Locate and identify every blood parasite.
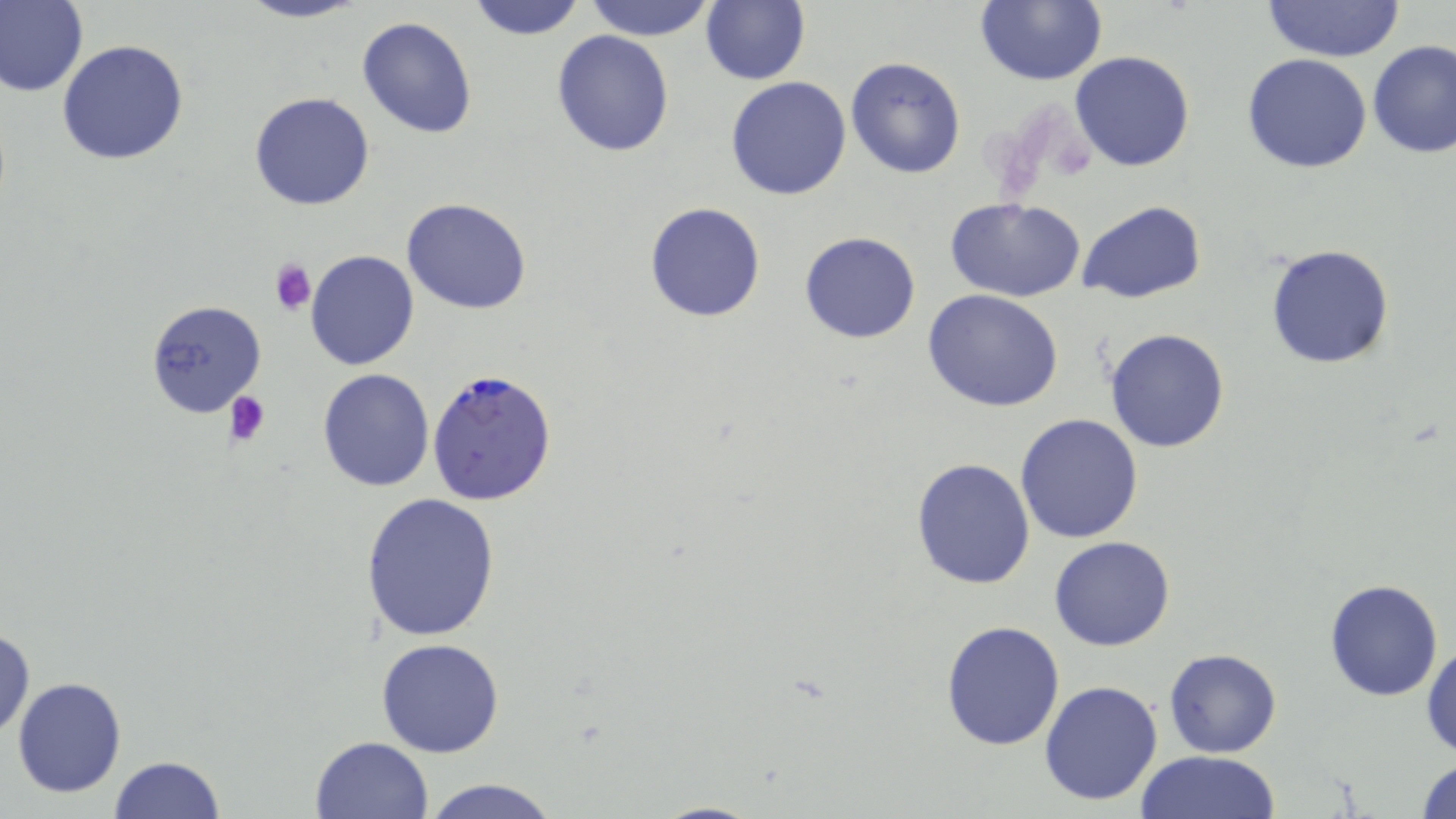
Approximate bounding boxes as named x1/y1/x2/y2 corners in pixels.
Plasmodium falciparum-infected red blood cells: (x1=426, y1=367, x2=558, y2=507).
No Plasmodium ovale, Plasmodium malariae, Plasmodium vivax, Babesia divergens, or Trypanosoma brucei observed.

Platelet locations: (x1=270, y1=258, x2=317, y2=314), (x1=224, y1=391, x2=273, y2=446). Uninfected red blood cell locations: (x1=0, y1=0, x2=88, y2=98), (x1=233, y1=0, x2=371, y2=24), (x1=464, y1=0, x2=588, y2=40), (x1=581, y1=0, x2=719, y2=40), (x1=700, y1=0, x2=810, y2=85), (x1=973, y1=1, x2=1107, y2=87), (x1=1263, y1=1, x2=1406, y2=63), (x1=356, y1=16, x2=480, y2=138), (x1=552, y1=30, x2=675, y2=157), (x1=57, y1=39, x2=190, y2=166), (x1=1367, y1=40, x2=1456, y2=158), (x1=1069, y1=50, x2=1197, y2=172), (x1=1241, y1=54, x2=1372, y2=174), (x1=844, y1=56, x2=967, y2=180), (x1=725, y1=77, x2=852, y2=201), (x1=248, y1=92, x2=376, y2=211), (x1=401, y1=197, x2=531, y2=315), (x1=945, y1=197, x2=1086, y2=302), (x1=1077, y1=201, x2=1204, y2=304), (x1=644, y1=202, x2=767, y2=323), (x1=799, y1=231, x2=922, y2=344), (x1=1265, y1=242, x2=1397, y2=370), (x1=305, y1=250, x2=418, y2=370), (x1=922, y1=290, x2=1064, y2=411), (x1=146, y1=300, x2=268, y2=418), (x1=1103, y1=327, x2=1231, y2=453), (x1=316, y1=369, x2=435, y2=492), (x1=1015, y1=413, x2=1143, y2=543), (x1=911, y1=458, x2=1036, y2=590), (x1=358, y1=490, x2=499, y2=640), (x1=1049, y1=536, x2=1176, y2=651), (x1=1323, y1=577, x2=1443, y2=701), (x1=941, y1=620, x2=1067, y2=752), (x1=0, y1=625, x2=35, y2=743), (x1=375, y1=638, x2=505, y2=758), (x1=1421, y1=639, x2=1455, y2=760), (x1=1164, y1=649, x2=1282, y2=758), (x1=12, y1=677, x2=127, y2=799), (x1=1040, y1=680, x2=1164, y2=806), (x1=310, y1=736, x2=436, y2=819), (x1=1134, y1=750, x2=1282, y2=819), (x1=108, y1=756, x2=225, y2=819), (x1=1412, y1=757, x2=1456, y2=818), (x1=420, y1=777, x2=562, y2=819), (x1=647, y1=799, x2=766, y2=819). Slide-level diagnosis: Plasmodium falciparum. One field of a larger specimen. Image is 1456×819 pixels. Optical microscopy. Thin blood smear. Captured at 1000x magnification. May-Grünwald-Giemsa stain.